Point out each Plasmodium parasite.
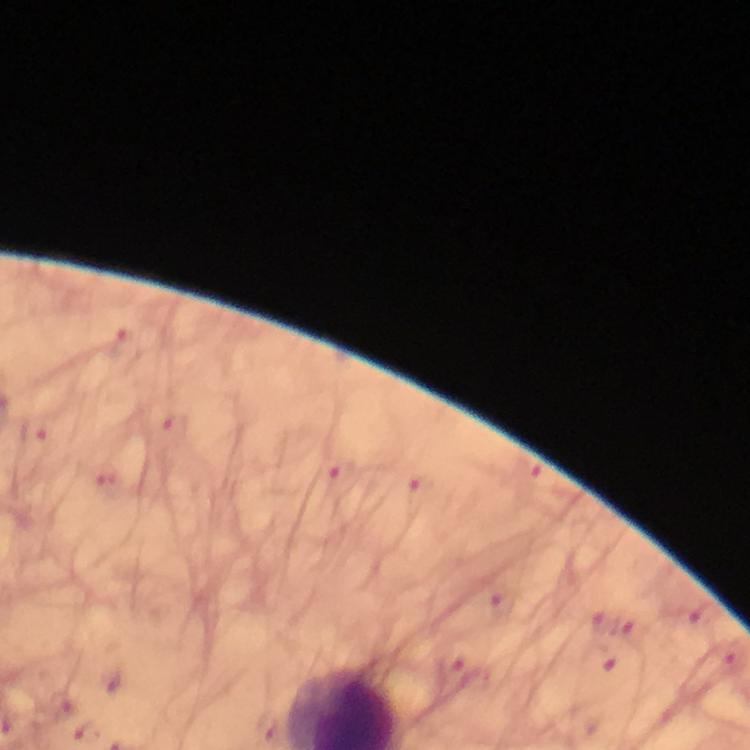

Approximate object centers, in pixels from the top-left corner.
Plasmodium parasites: (x=123, y=348), (x=175, y=428), (x=33, y=431), (x=341, y=482), (x=417, y=496).

At 100x magnification. Immersion oil applied. Cropped region of a single field of view. Smartphone photograph taken through a microscope. Giemsa-stained preparation. From a diagnostic examination for malaria. Thick blood film. Image is 750×750 pixels.